Report the malaria status of this cell.
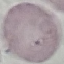

Uninfected.

{
  "capture": "smartphone through the microscope eyepiece",
  "stain": "Giemsa",
  "preparation": "thin smear",
  "image_type": "automatically extracted cell patch, resized to 64 × 64 pixels"
}